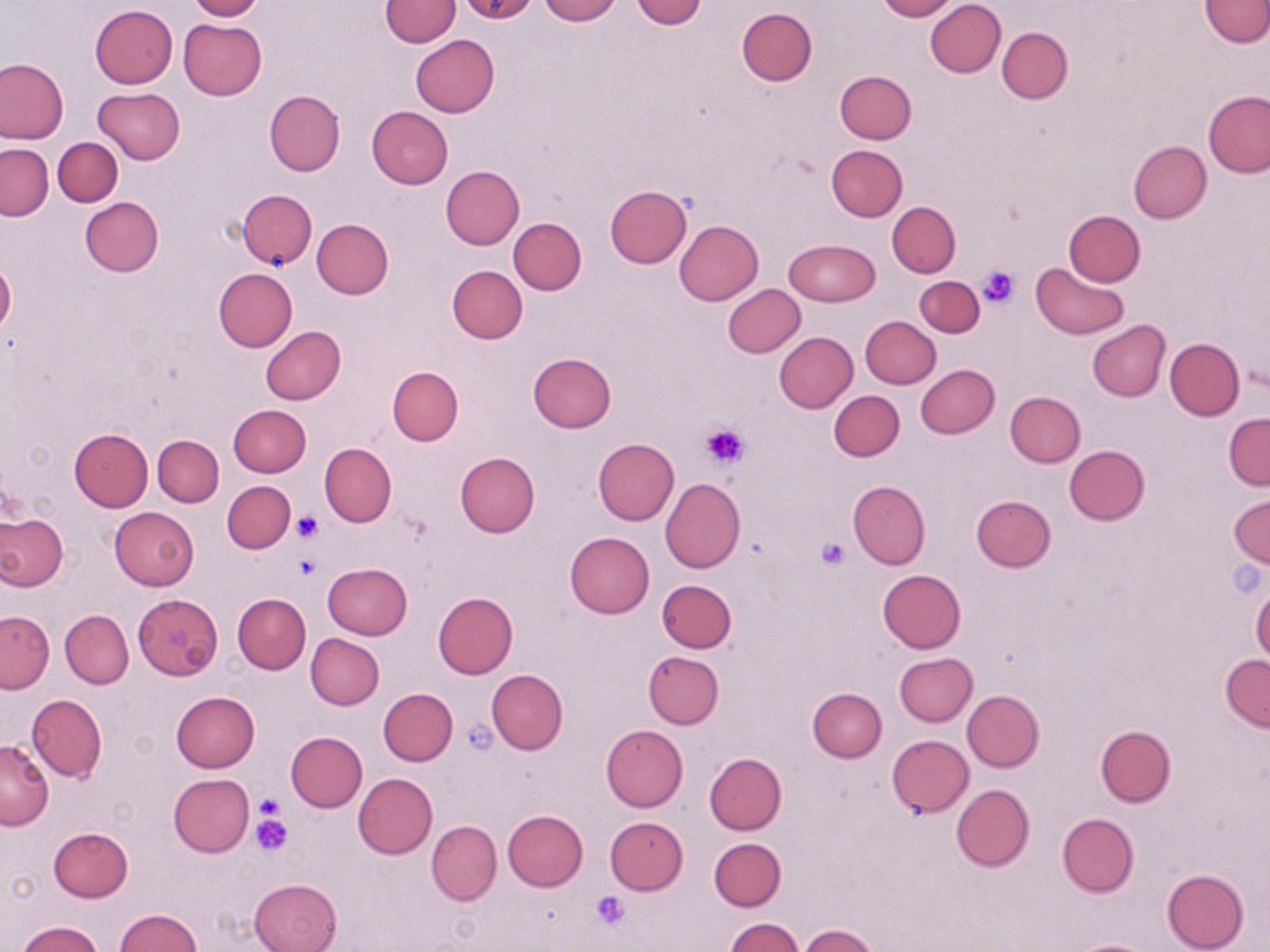 Approximate bounding boxes as [x1, y1, x2, y2] in pixels. Platelet locations: [977, 263, 1020, 308], [701, 425, 750, 468], [292, 512, 321, 541], [816, 537, 848, 570], [291, 553, 321, 581], [463, 719, 500, 755], [254, 794, 282, 824], [250, 814, 291, 857], [590, 890, 631, 929]. Uninfected red blood cell locations: [187, 0, 265, 21], [379, 0, 461, 47], [455, 0, 539, 25], [537, 0, 620, 24], [632, 0, 707, 28], [874, 0, 957, 21], [924, 0, 1005, 77], [1198, 0, 1270, 47], [89, 5, 178, 88], [736, 6, 817, 86], [179, 19, 267, 100], [997, 27, 1073, 103], [411, 36, 500, 116], [1, 57, 68, 144], [835, 71, 917, 144], [93, 87, 185, 163], [265, 90, 345, 176], [1203, 90, 1270, 178], [366, 106, 453, 188], [53, 137, 123, 206], [1128, 141, 1211, 223], [1, 144, 52, 220], [826, 144, 908, 222], [441, 165, 524, 249], [606, 185, 690, 267], [238, 189, 317, 269], [80, 197, 163, 277], [887, 202, 960, 277], [1063, 210, 1145, 286], [313, 218, 394, 298], [509, 218, 586, 295], [674, 220, 763, 305], [785, 239, 879, 305], [0, 258, 16, 337], [1032, 261, 1128, 340], [447, 265, 527, 344], [213, 268, 297, 352], [915, 276, 984, 336], [723, 285, 806, 357], [860, 316, 940, 389], [1087, 320, 1171, 402], [260, 326, 346, 404], [773, 332, 857, 413], [1164, 337, 1243, 420], [528, 352, 616, 432], [916, 363, 999, 438], [386, 366, 463, 446], [829, 390, 904, 461], [1005, 391, 1084, 467], [228, 404, 311, 477], [1223, 412, 1269, 490], [69, 429, 153, 511], [152, 435, 224, 506], [593, 438, 679, 524], [319, 442, 397, 526], [1064, 445, 1150, 525], [454, 450, 539, 537], [660, 479, 745, 573], [847, 480, 930, 568], [222, 481, 295, 554], [1228, 493, 1269, 567], [971, 496, 1055, 572], [111, 507, 198, 590], [0, 512, 66, 590], [565, 531, 654, 618], [324, 562, 412, 639], [877, 569, 966, 653], [657, 579, 735, 653], [233, 593, 311, 673], [434, 593, 518, 677], [133, 594, 223, 680], [61, 610, 133, 688], [1, 611, 54, 692], [306, 634, 384, 709], [644, 651, 724, 729], [893, 653, 977, 727], [1220, 654, 1269, 731], [486, 668, 568, 754], [378, 687, 458, 765], [807, 687, 887, 762], [962, 689, 1044, 772], [171, 691, 260, 772], [27, 694, 107, 783], [601, 724, 687, 811], [1096, 725, 1175, 806], [285, 731, 367, 812], [887, 734, 973, 818], [0, 740, 54, 830], [705, 752, 787, 834], [353, 773, 437, 858], [168, 774, 254, 857], [951, 784, 1034, 871], [502, 810, 587, 890], [1057, 813, 1139, 896], [605, 816, 688, 894], [427, 820, 502, 904], [49, 826, 133, 901], [709, 838, 786, 911], [1162, 869, 1250, 952], [250, 877, 342, 952], [116, 908, 202, 951], [723, 917, 803, 951], [17, 921, 104, 952], [797, 924, 880, 952], [1068, 939, 1160, 952]. Slide-level diagnosis: no evidence of blood parasites. Thin blood film. Light microscopy. One field of a larger specimen. Image is 1270×952 pixels. May-Grünwald-Giemsa stain. Captured at 1000x magnification.